Report the malaria status of this cell.
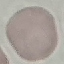

It is uninfected.

Summary:
  - Image type: automatically extracted cell patch, resized to 64 × 64 pixels
  - Stain: Giemsa
  - Capture: smartphone through the microscope eyepiece
  - Preparation: thin blood smear